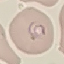
Malaria status: parasitized. Acquired by smartphone through the microscope eyepiece. Cell patch, automatically extracted from a larger field of view and resized to 64 × 64 pixels. Thin blood film. Giemsa-stained preparation.